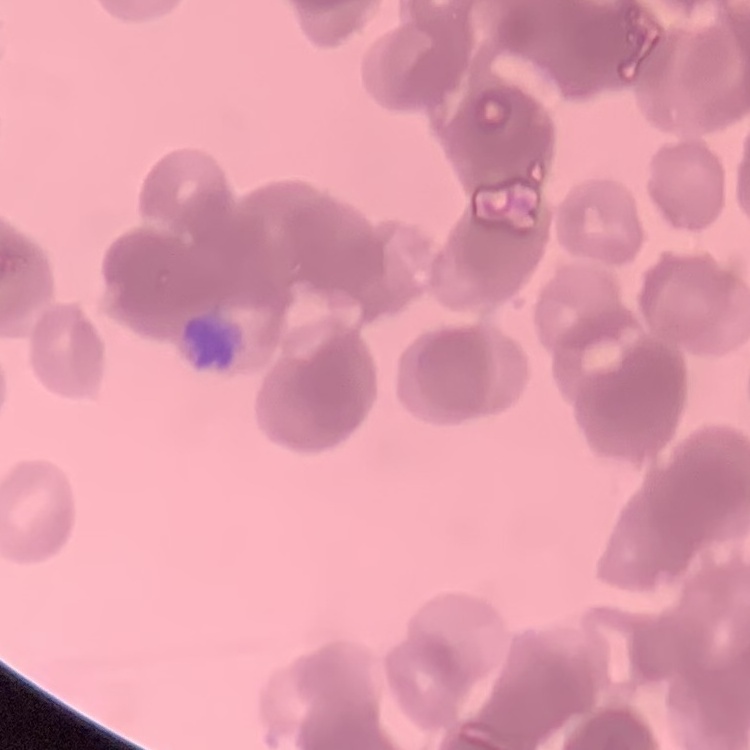

Summary:
  - Red blood cell morphology: rouleaux formation
  - Stain: Field's or Giemsa
  - Preparation: thin blood smear
  - Image type: square crop of a larger photomicrograph